Outline each blood parasite and name the species.
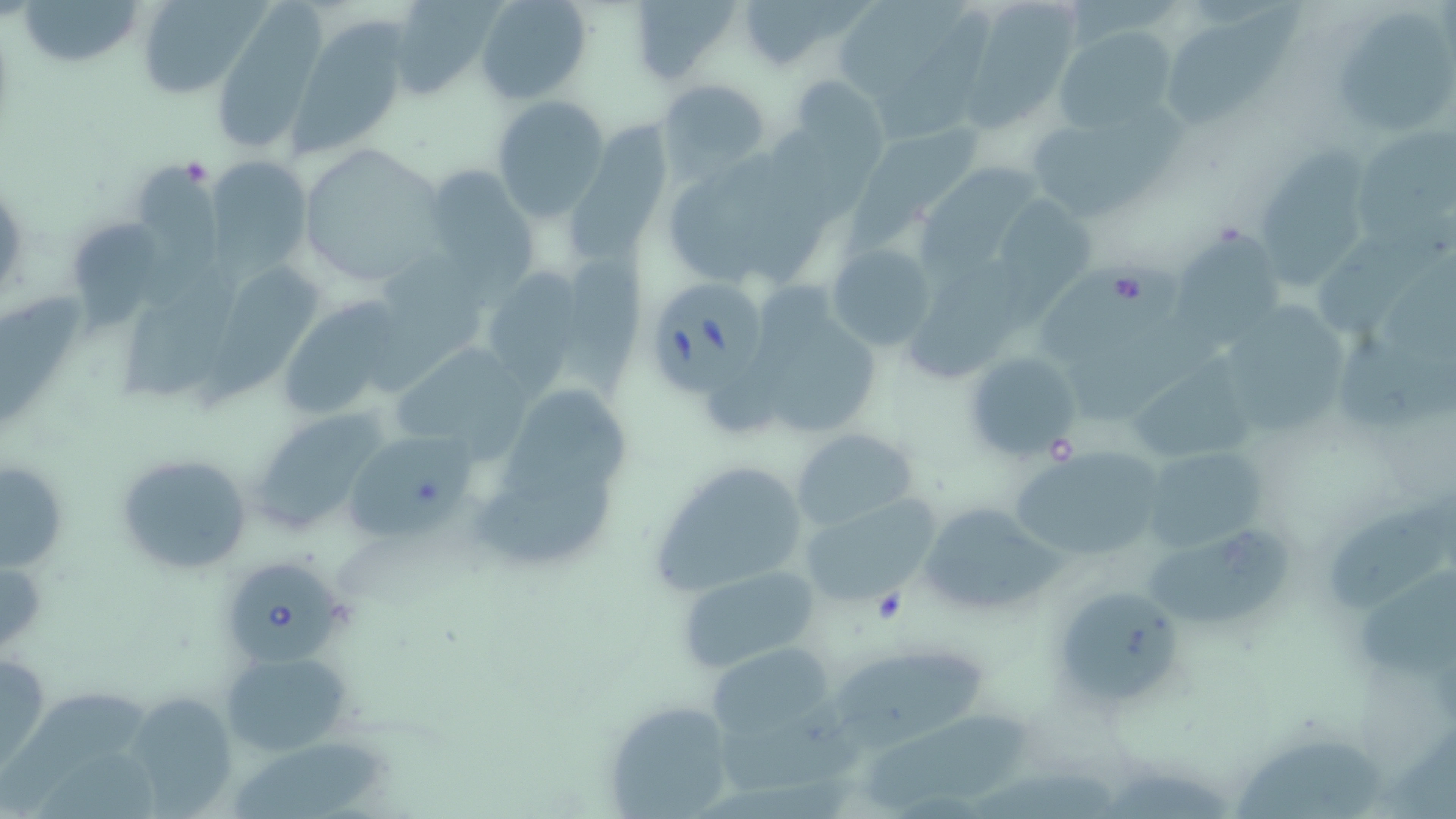
Approximate bounding boxes as (x1,y1)-(x2,y2) corner pairs in pixels.
Babesia divergens-infected red blood cells: (649,278)-(765,401), (226,557)-(345,665).
No Plasmodium falciparum, Plasmodium ovale, Plasmodium malariae, Plasmodium vivax, or Trypanosoma brucei observed.

{
  "slide_level_diagnosis": "Babesia divergens",
  "field_of_view": "single",
  "preparation": "thin blood smear",
  "platelet_locations": "approximate bounding boxes as (x1,y1)-(x2,y2) corner pairs in pixels: (867,590)-(908,626)",
  "magnification": "1000x",
  "image_size": "1456×819 pixels",
  "stain": "May-Grünwald-Giemsa",
  "modality": "light microscopy",
  "uninfected_red_blood_cell_locations": "approximate bounding boxes as (x1,y1)-(x2,y2) corner pairs in pixels: (23,0)-(141,70), (136,0)-(266,100), (385,0)-(503,98), (476,0)-(593,106), (625,0)-(739,85), (735,0)-(852,71), (831,0)-(981,98), (968,2)-(1086,135), (1160,2)-(1307,131), (1337,13)-(1456,133), (293,19)-(411,160), (1054,28)-(1180,134), (788,75)-(886,171), (656,77)-(771,177), (492,96)-(610,222), (1035,110)-(1186,217), (562,111)-(677,281), (1354,123)-(1456,248), (866,130)-(985,225), (296,146)-(447,287), (1260,149)-(1373,296), (207,158)-(314,269), (133,159)-(224,320), (422,165)-(540,290), (925,165)-(1044,283), (1001,197)-(1095,327), (75,214)-(168,343), (1314,214)-(1456,338), (1172,228)-(1281,341), (826,243)-(937,351), (362,247)-(492,398), (1043,247)-(1227,430), (563,248)-(650,413), (909,257)-(1032,381), (491,259)-(586,401), (121,261)-(241,408), (208,263)-(327,406), (0,286)-(90,430), (283,299)-(401,414), (1229,304)-(1349,436), (387,342)-(535,472), (962,350)-(1082,462), (1129,360)-(1254,470), (496,393)-(637,505), (252,413)-(386,534), (792,427)-(919,532), (343,432)-(483,544), (1140,446)-(1272,553), (1006,447)-(1163,563), (113,452)-(256,575), (649,458)-(816,596), (1,460)-(68,574), (471,472)-(618,554), (794,491)-(942,611), (1329,495)-(1456,617), (916,500)-(1063,617), (1145,535)-(1299,635), (677,565)-(820,673), (1357,570)-(1456,680), (1064,599)-(1176,702), (712,641)-(838,737), (0,648)-(48,780), (221,650)-(350,756), (835,650)-(993,765), (0,689)-(147,818), (706,692)-(878,796), (134,694)-(248,819), (601,699)-(739,818), (863,712)-(1042,816), (1240,739)-(1386,819), (225,741)-(387,819)"
}